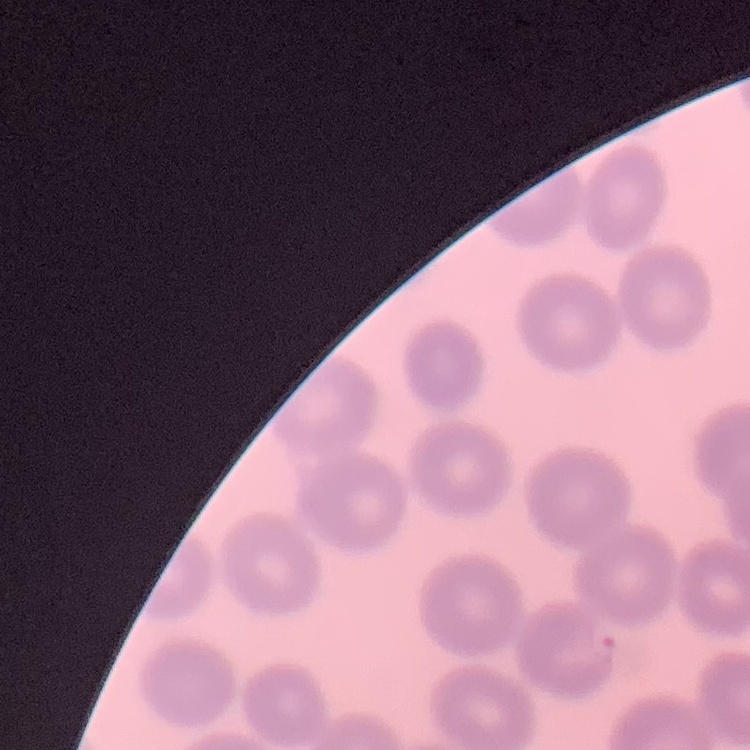
The erythrocytes exhibit no rouleaux formation. Stained with either Field's or Giemsa. Square crop of a larger photomicrograph. Thin blood film.